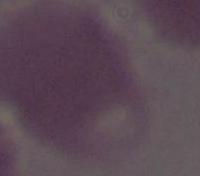
Summary:
  - Modality: photomicrograph
  - Identification: red blood cell
  - Magnification: 1000x